Assess this cell for malaria.
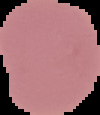
Uninfected.

Summary:
  - Preparation: thin blood smear
  - Image type: segmented cell region with the area outside set to black
  - Image size: 100×115 pixels